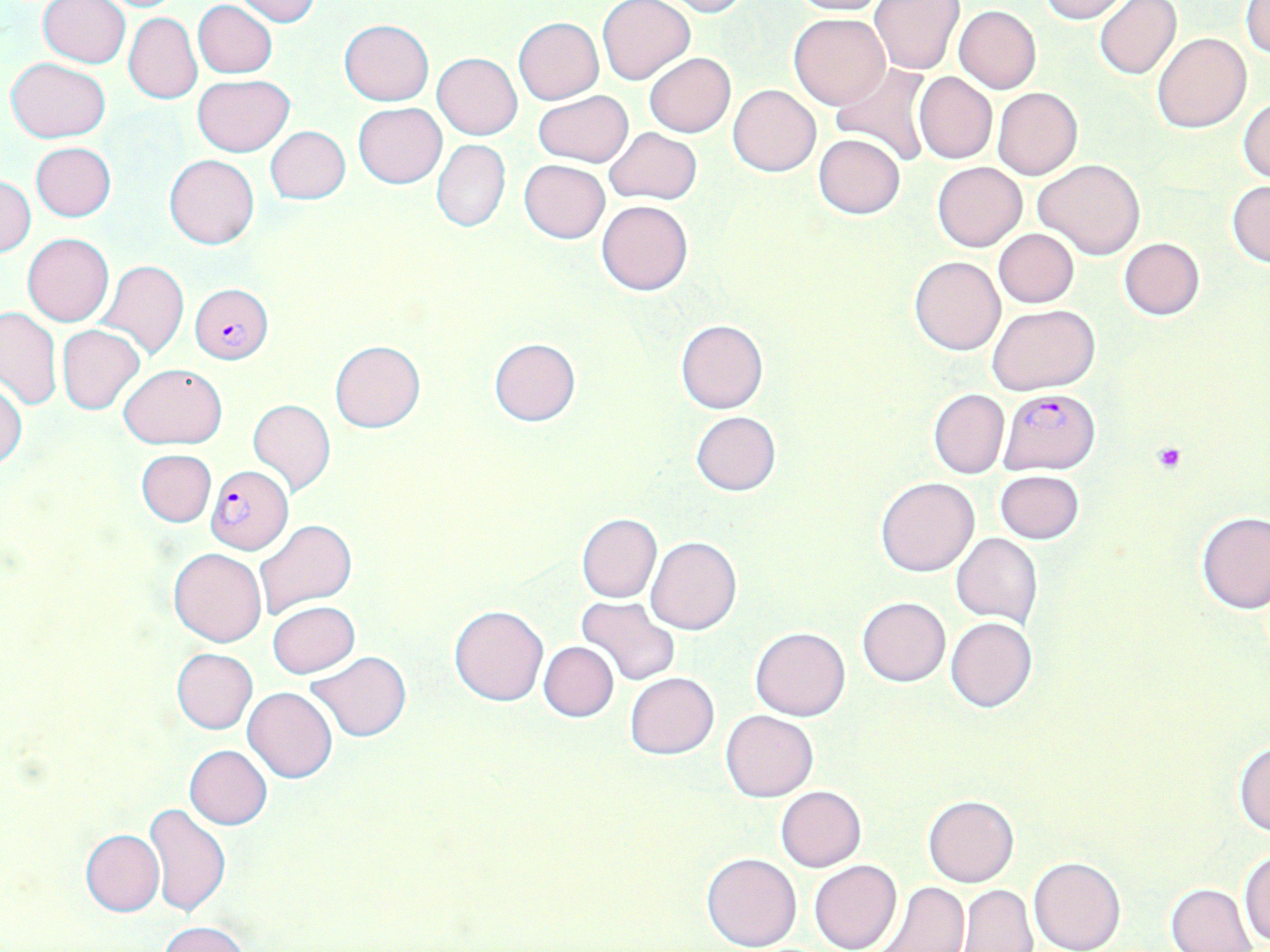 Approximate bounding boxes as (x1, y1, x2, y2) in pixels. Plasmodium falciparum-infected red blood cell locations: (190, 284, 273, 364), (998, 388, 1100, 474), (206, 466, 293, 554). Uninfected red blood cell locations: (38, 0, 130, 67), (233, 0, 320, 24), (784, 0, 890, 16), (1038, 0, 1129, 23), (1094, 0, 1182, 80), (598, 1, 694, 86), (662, 1, 749, 17), (869, 1, 963, 74), (1243, 1, 1270, 57), (194, 2, 278, 78), (954, 6, 1042, 93), (125, 9, 277, 89), (788, 12, 890, 109), (123, 13, 202, 104), (513, 17, 604, 103), (338, 19, 433, 105), (1152, 33, 1251, 133), (643, 52, 735, 138), (433, 53, 522, 139), (6, 58, 112, 142), (831, 64, 935, 167), (914, 72, 996, 163), (193, 74, 294, 157), (729, 84, 819, 177), (993, 87, 1082, 180), (533, 90, 633, 166), (1237, 96, 1270, 183), (354, 102, 446, 188), (265, 125, 350, 203), (604, 127, 702, 204), (815, 134, 905, 218), (432, 140, 510, 232), (31, 142, 116, 221), (164, 154, 258, 249), (1032, 158, 1146, 261), (519, 160, 609, 244), (933, 161, 1027, 251), (1, 176, 35, 256), (1226, 181, 1270, 267), (597, 199, 692, 295), (994, 229, 1079, 307), (22, 234, 113, 326), (1119, 238, 1205, 320), (910, 257, 1004, 355), (100, 260, 188, 361), (988, 305, 1098, 395), (0, 309, 61, 410), (676, 318, 768, 414), (58, 324, 145, 414), (489, 338, 581, 426), (329, 340, 425, 432), (120, 364, 224, 448), (0, 380, 26, 470), (928, 388, 1009, 479), (248, 398, 336, 497), (690, 411, 780, 496), (136, 449, 217, 527), (994, 469, 1084, 544), (877, 477, 979, 577), (1196, 511, 1269, 614), (576, 513, 662, 602), (254, 520, 358, 620), (952, 532, 1042, 627), (646, 536, 742, 634), (168, 549, 267, 647), (577, 596, 680, 686), (857, 596, 951, 686), (267, 600, 360, 678), (449, 605, 549, 706), (945, 617, 1037, 712), (750, 626, 850, 721), (538, 641, 619, 722), (171, 648, 257, 733), (305, 651, 413, 740), (625, 672, 719, 759), (243, 686, 337, 782), (721, 710, 817, 801), (1234, 740, 1270, 836), (185, 745, 272, 829), (776, 785, 867, 872), (923, 795, 1018, 887), (145, 803, 231, 917), (81, 829, 164, 917), (1240, 848, 1270, 946), (702, 851, 801, 951), (1028, 856, 1125, 952), (809, 860, 900, 952), (874, 882, 970, 952), (957, 884, 1037, 952), (1168, 884, 1258, 952), (160, 921, 248, 952). Platelet locations: (1152, 442, 1187, 473). Slide-level diagnosis: Plasmodium falciparum. Optical microscopy. One field of a larger specimen. May-Grünwald-Giemsa stain. 1000x magnification. Thin blood smear. Image is 1270×952 pixels.